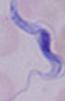

Micrograph. A trypanosome is seen. 1000x magnification.